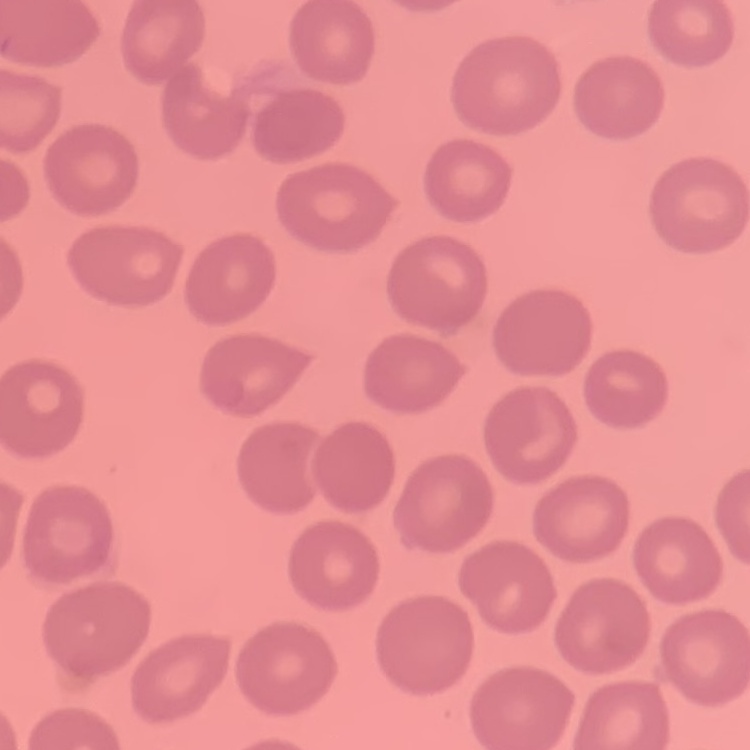

erythrocyte morphology = no rouleaux formation
stain = Field's or Giemsa
image type = square crop of a larger photomicrograph
preparation = thin peripheral smear